Give the position of every Plasmodium parasite.
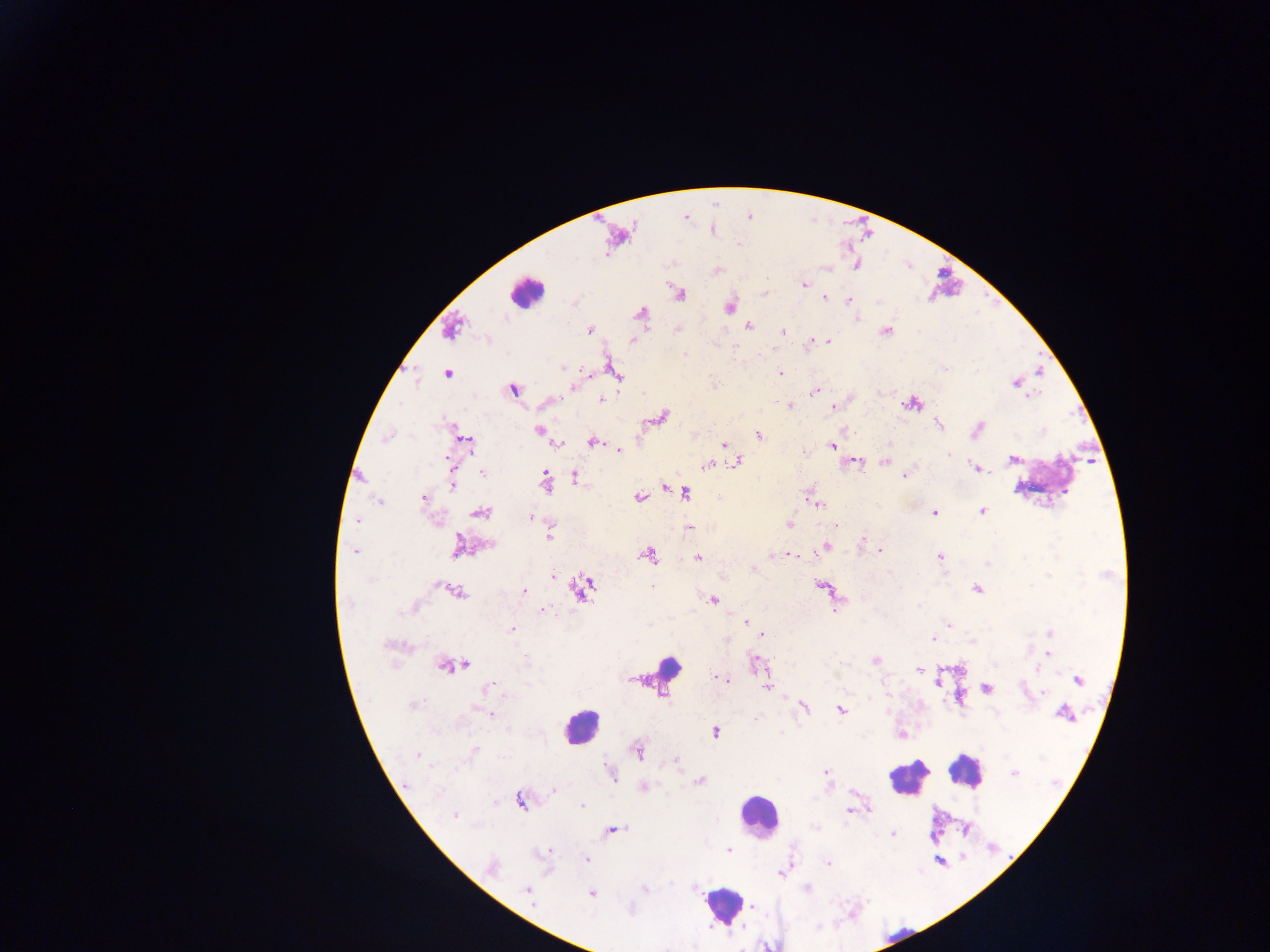
Approximate centers as (x, y) in pixels.
Plasmodium parasites: (685, 217), (711, 229), (617, 235), (717, 270), (804, 285), (764, 292), (678, 293), (823, 297), (849, 300), (729, 306), (640, 313), (856, 318), (748, 325), (451, 329), (589, 329), (677, 329), (885, 331), (782, 332), (487, 339), (631, 340), (828, 340), (811, 341), (563, 367), (612, 369), (447, 373), (589, 373), (780, 374), (615, 375), (1015, 382), (574, 385), (513, 390), (814, 391), (601, 400), (548, 402), (912, 403), (790, 406), (831, 406), (661, 416), (937, 423), (451, 428), (977, 429), (538, 430), (758, 435), (386, 438), (465, 441), (592, 442), (558, 443), (724, 444), (831, 445), (618, 449), (948, 454), (1012, 459), (736, 462), (855, 462), (884, 462), (719, 463), (707, 465), (978, 468), (481, 471), (453, 472), (575, 476), (903, 476), (544, 480), (453, 481), (664, 486), (685, 492), (811, 496), (639, 497), (718, 497), (423, 498), (379, 501), (817, 502), (982, 510), (479, 512), (934, 512), (530, 516), (356, 520), (789, 524), (837, 526), (688, 528), (550, 531), (862, 539), (487, 544), (457, 546), (825, 546), (879, 550), (355, 551), (788, 553), (648, 554), (940, 557), (697, 558), (752, 568), (552, 576), (821, 585), (581, 587), (976, 589), (454, 590), (524, 591), (713, 599), (836, 606), (542, 609), (745, 621), (948, 624), (511, 629), (762, 633), (1049, 633), (932, 638), (393, 645), (1047, 653), (875, 660), (757, 663), (461, 664), (450, 665), (918, 669), (938, 677), (722, 679), (1077, 680), (766, 681), (986, 687), (488, 688), (1044, 692), (413, 704), (803, 707), (840, 708), (1065, 712), (490, 714), (715, 732), (900, 733), (474, 750), (637, 751), (675, 760), (826, 773), (1013, 773), (611, 775), (699, 781), (643, 787), (553, 789), (520, 800), (581, 806), (850, 810), (455, 814), (966, 829), (612, 830), (893, 833), (728, 851), (547, 852), (586, 859), (828, 863), (491, 867), (528, 890), (590, 893), (752, 908).

country = Ghana
image size = 1270×952 pixels
field of view = single
preparation = thick blood smear
leukocyte locations = approximate centers as (x, y) in pixels: (527, 293), (1047, 479), (663, 673), (581, 726), (964, 770), (908, 776), (758, 816), (723, 904), (900, 935), (769, 944)
capture = mobile-phone photograph through a microscope